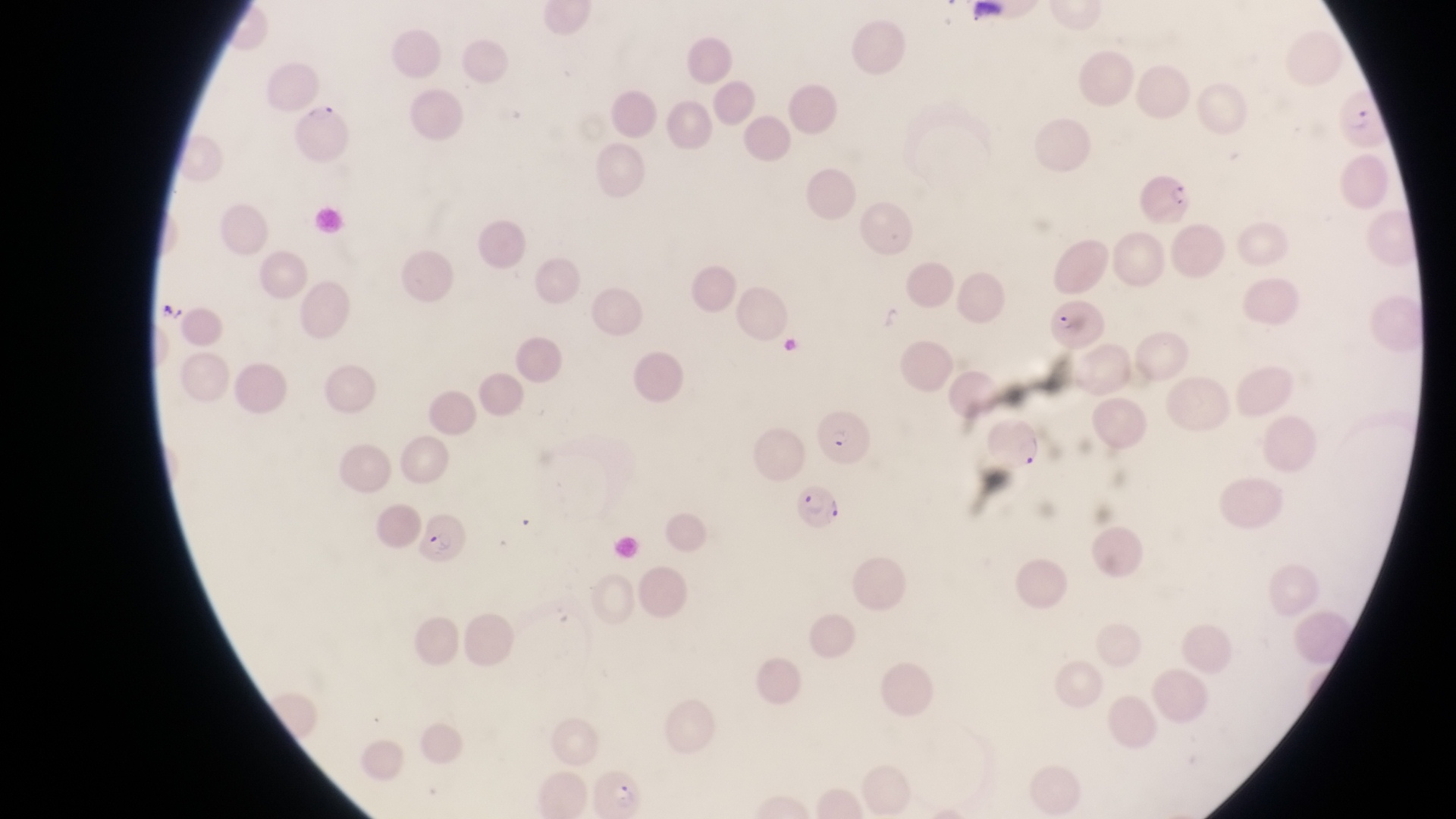 Approximate bounding boxes as left top right bottom in pixels. Artifact (platelet-like body, stain precipitate, or debris) locations: 155 300 181 329; 875 301 911 340; 777 336 809 355. Parasitised red blood cell locations: 1340 85 1390 148; 294 99 354 163; 1141 168 1196 229; 1050 296 1106 354; 984 410 1043 474; 809 415 873 468; 796 479 845 542; 416 507 466 568; 589 770 644 816. Magnification of 1000x. Photographed through the eyepiece of an Olympus CX-23 microscope with a smartphone camera. Single field of view. Thin blood smear. Image is 1456×819 pixels. Sample from Uganda.